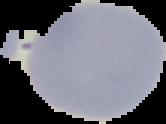
From a thin blood film. Image is 166×124 pixels. Malaria status: uninfected. Cell region segmented out of the field of view; the surrounding area is masked to black.